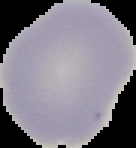 Image is 136×148 pixels. Result: no Plasmodium parasites seen. Segmented cell region on a black background. From a thin blood film.